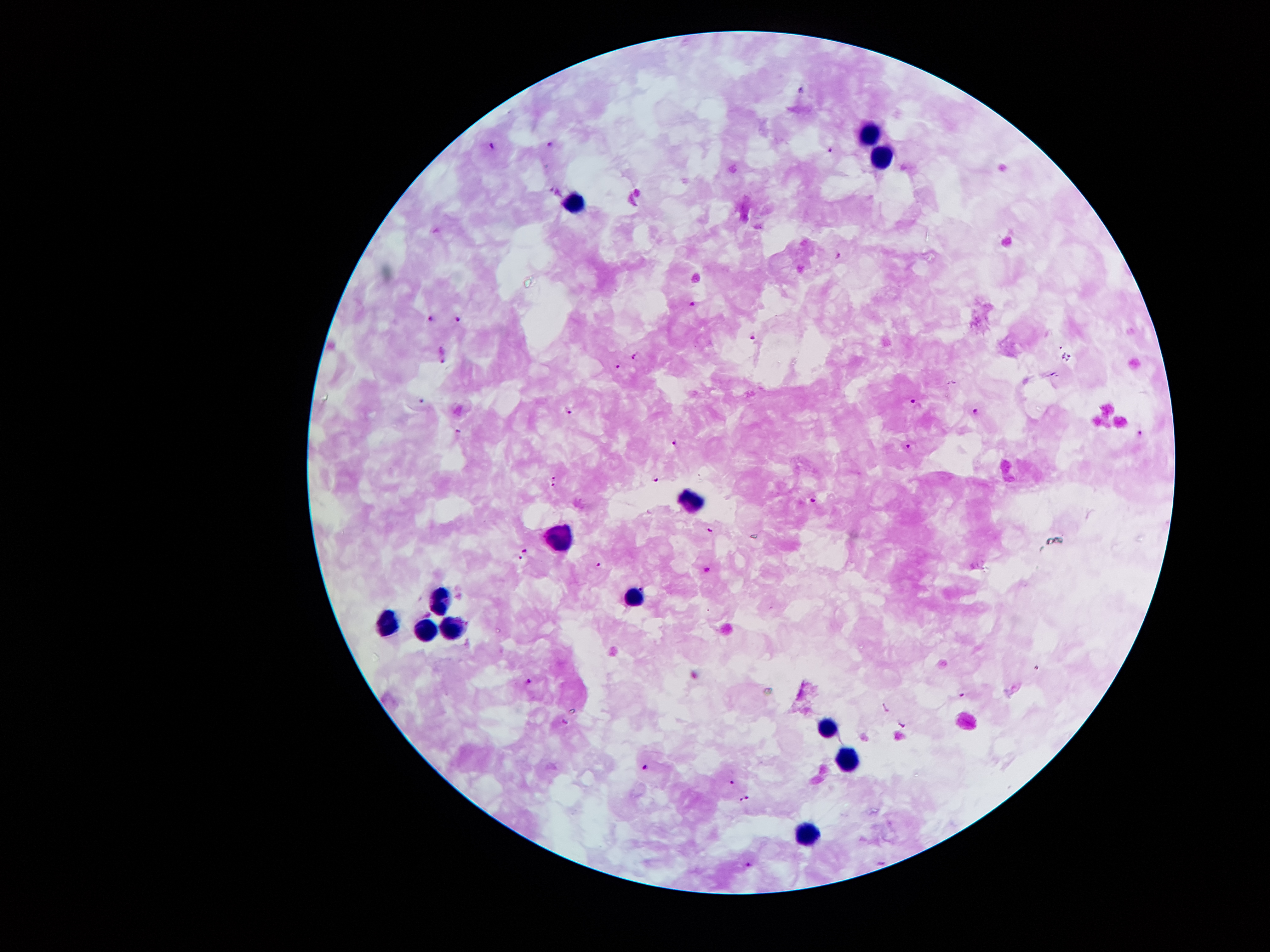

Approximate centers as [x, y] in pixels.
Summary:
  - Malaria parasite locations: [801, 90], [548, 143], [494, 145], [829, 148], [841, 254], [693, 303], [430, 318], [458, 319], [753, 336], [443, 354], [637, 357], [1067, 357], [618, 368], [915, 400], [423, 402], [975, 410], [569, 412], [459, 431], [1140, 434], [675, 442], [909, 445], [555, 475], [654, 480], [552, 484], [813, 500], [710, 529], [524, 550], [521, 557], [598, 566], [706, 570], [643, 587], [530, 680], [962, 695], [886, 707], [903, 724], [645, 766], [732, 784], [749, 797], [743, 800], [749, 864]
  - Leukocyte locations: [871, 134], [879, 153], [572, 205], [691, 500], [564, 539], [441, 597], [633, 602], [388, 625], [426, 626], [452, 626], [827, 723], [850, 760], [804, 835]
  - Preparation: thick blood film
  - Magnification: 100x
  - Field of view: single
  - Stain: Giemsa
  - Capture: smartphone through the microscope eyepiece
  - Image size: 1270×952 pixels
  - Patient malaria status: positive for Plasmodium falciparum